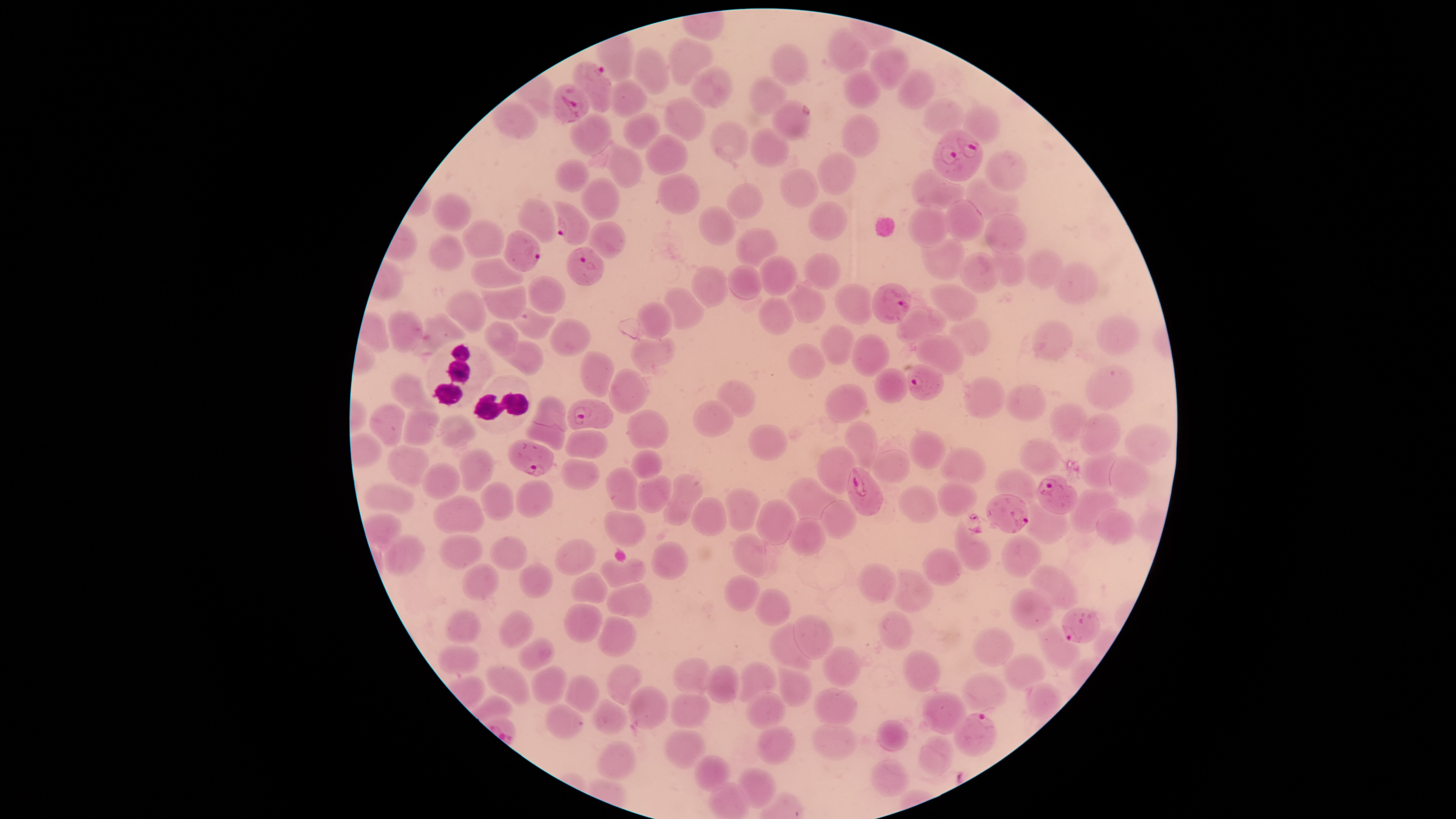 Approximate bounding boxes as [left, top, right, bottom] in pixels. Parasitized red blood cells: [573, 62, 611, 113], [553, 83, 589, 123], [932, 129, 983, 181], [552, 201, 590, 244], [503, 231, 540, 269], [567, 247, 604, 285], [872, 284, 911, 324], [908, 364, 944, 400], [567, 400, 613, 430], [509, 440, 554, 476], [847, 468, 883, 516], [1036, 474, 1077, 514], [986, 494, 1029, 533], [1062, 608, 1100, 643], [955, 713, 997, 756]. Uninfected red blood cells: [827, 29, 870, 73], [666, 37, 714, 86], [770, 44, 809, 87], [870, 45, 909, 90], [632, 46, 670, 94], [690, 67, 732, 107], [843, 69, 884, 108], [896, 69, 936, 110], [749, 77, 788, 116], [609, 80, 648, 119], [664, 98, 708, 140], [924, 99, 963, 134], [771, 100, 812, 141], [490, 101, 538, 139], [962, 107, 998, 145], [623, 113, 660, 150], [570, 114, 611, 155], [841, 115, 880, 158], [709, 121, 750, 163], [749, 128, 790, 167], [643, 133, 687, 176], [593, 143, 643, 190], [983, 150, 1027, 192], [817, 152, 858, 195], [555, 159, 590, 193], [779, 168, 819, 208], [911, 170, 964, 211], [656, 172, 699, 215], [580, 177, 622, 219], [964, 177, 1020, 220], [726, 184, 762, 219], [432, 193, 471, 232], [517, 198, 557, 244], [946, 200, 985, 240], [808, 202, 847, 240], [698, 205, 736, 246], [909, 207, 949, 247], [984, 214, 1028, 255], [463, 219, 506, 258], [589, 222, 627, 258], [737, 228, 778, 268], [430, 234, 465, 270], [920, 238, 965, 280], [990, 249, 1027, 286], [1026, 249, 1064, 289], [960, 251, 999, 293], [804, 253, 841, 290], [758, 257, 798, 296], [471, 259, 523, 289], [1053, 262, 1098, 305], [728, 264, 763, 299], [691, 265, 728, 307], [526, 276, 566, 314], [788, 281, 826, 322], [931, 283, 979, 320], [834, 284, 874, 325], [480, 285, 527, 321], [664, 287, 704, 330], [446, 292, 486, 331], [757, 296, 795, 336], [638, 302, 672, 339], [505, 305, 555, 341], [895, 305, 948, 345], [388, 310, 423, 351], [424, 314, 467, 343], [1097, 315, 1139, 356], [549, 318, 589, 357], [950, 319, 991, 355], [486, 320, 518, 354], [1031, 320, 1074, 362], [821, 325, 855, 365], [915, 333, 964, 376], [852, 334, 889, 378], [630, 338, 676, 375], [497, 340, 542, 374], [788, 344, 825, 378], [580, 352, 614, 398], [1086, 365, 1135, 411], [874, 368, 908, 404], [608, 369, 649, 415], [390, 372, 438, 410], [964, 377, 1005, 418], [718, 379, 756, 417], [824, 383, 868, 423], [1005, 384, 1046, 421], [533, 396, 566, 430], [693, 400, 734, 437], [1049, 403, 1088, 444], [368, 404, 405, 446], [402, 410, 440, 445], [626, 410, 668, 450], [439, 414, 476, 448], [1079, 414, 1121, 455], [526, 421, 566, 450], [845, 421, 878, 469], [1124, 424, 1171, 464], [747, 425, 787, 460], [564, 430, 607, 459], [909, 430, 947, 470], [1020, 438, 1059, 475], [387, 445, 431, 488], [816, 446, 856, 495], [940, 447, 986, 484], [458, 448, 495, 493], [631, 449, 662, 479], [872, 450, 911, 483], [1080, 451, 1118, 489], [1109, 457, 1149, 499], [561, 458, 600, 491], [420, 463, 460, 502], [606, 467, 638, 513], [995, 469, 1039, 504], [662, 473, 702, 526], [637, 475, 672, 513], [787, 476, 837, 520], [516, 479, 553, 517], [937, 481, 978, 517], [481, 483, 514, 522], [365, 484, 415, 515], [897, 485, 939, 524], [724, 488, 761, 532], [1071, 489, 1118, 532], [433, 496, 483, 533], [691, 497, 728, 536], [756, 500, 795, 546], [821, 501, 856, 538], [1024, 503, 1068, 540], [1098, 509, 1132, 545], [605, 510, 646, 547], [790, 518, 827, 556], [953, 519, 992, 570], [384, 534, 427, 575], [438, 534, 483, 568], [732, 534, 765, 578], [1001, 535, 1041, 578], [489, 536, 528, 571], [556, 539, 595, 576], [652, 542, 689, 581], [923, 549, 961, 586], [601, 558, 647, 586], [517, 562, 553, 601], [461, 564, 500, 601], [857, 564, 896, 602], [1030, 565, 1079, 611], [890, 569, 933, 612], [570, 572, 608, 604], [724, 574, 759, 612], [607, 583, 652, 618], [1010, 588, 1053, 631], [755, 589, 792, 625], [564, 604, 603, 644], [447, 609, 481, 645], [497, 609, 535, 648], [878, 610, 912, 651], [793, 615, 831, 659], [598, 616, 635, 656], [768, 622, 811, 671], [1039, 624, 1079, 668], [973, 628, 1014, 667], [517, 637, 555, 671], [438, 645, 480, 675], [821, 646, 862, 689], [903, 651, 941, 691], [1004, 653, 1044, 691], [675, 657, 710, 696], [739, 661, 776, 702], [776, 663, 812, 704], [605, 664, 642, 705], [706, 664, 739, 704], [487, 665, 532, 705], [531, 666, 568, 704], [961, 673, 1006, 712], [563, 675, 599, 713], [1025, 683, 1062, 721], [628, 686, 669, 729], [815, 688, 856, 725], [746, 692, 784, 729], [923, 692, 964, 735], [670, 693, 711, 728], [591, 700, 629, 734], [544, 705, 582, 739], [878, 718, 909, 752], [756, 726, 796, 764], [814, 726, 855, 760], [663, 728, 706, 770], [915, 736, 953, 779], [596, 741, 637, 781], [695, 755, 731, 792], [869, 760, 909, 797], [740, 768, 774, 808], [708, 783, 749, 819]. White blood cells: [425, 342, 495, 409], [472, 375, 533, 435]. Smartphone photograph through the microscope eyepiece. Giemsa stain. Image is 1456×819 pixels. Species: Plasmodium falciparum. Thin smear of blood. The visible region is circular. Single field of view. Presence: malaria parasites identified.